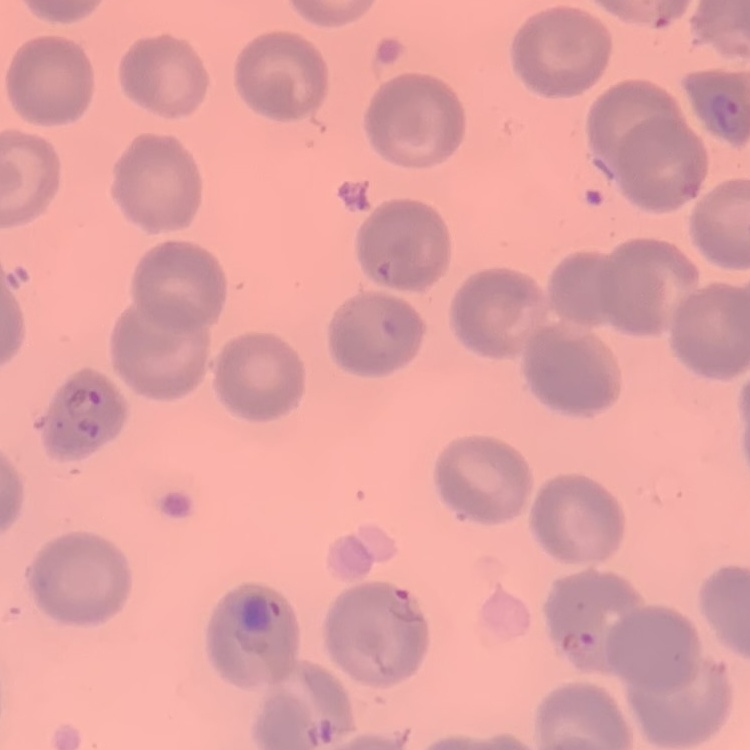

Summary:
  - Red blood cell morphology: no rouleaux formation
  - Image type: square crop of a larger photomicrograph
  - Stain: Field's or Giemsa
  - Preparation: thin blood smear